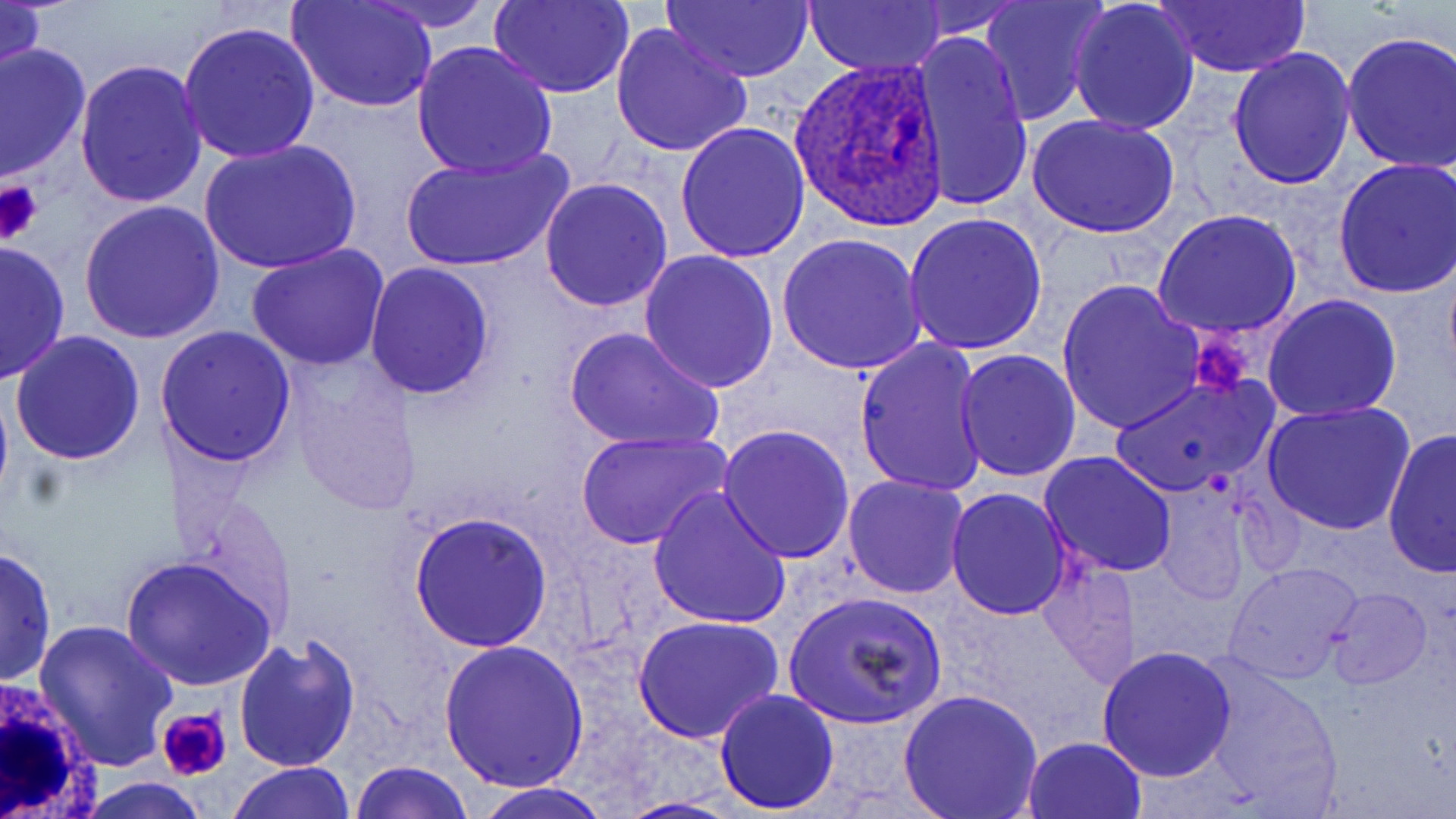

Approximate bounding boxes as (x1,y1)-(x2,y2) corner pairs in pixels. Platelet locations: (0,179)-(45,245), (1190,331)-(1255,399), (156,707)-(233,782). Plasmodium ovale-infected red blood cell locations: (790,57)-(950,229). White blood cell locations: (1,676)-(106,819). Uninfected red blood cell locations: (361,0)-(498,31), (490,0)-(633,99), (663,0)-(816,83), (805,0)-(946,77), (981,0)-(1106,124), (1068,0)-(1201,137), (1149,0)-(1312,76), (0,1)-(47,89), (289,1)-(439,113), (903,2)-(1029,39), (176,20)-(320,163), (610,24)-(752,158), (1341,30)-(1456,174), (911,31)-(1034,214), (412,40)-(557,179), (0,41)-(91,183), (1227,46)-(1356,190), (74,58)-(207,211), (1027,114)-(1179,241), (675,122)-(811,264), (198,138)-(362,274), (399,144)-(575,273), (1333,158)-(1456,301), (539,176)-(673,312), (77,199)-(226,344), (1152,208)-(1303,340), (902,214)-(1048,359), (777,235)-(926,376), (0,241)-(70,383), (248,243)-(387,371), (639,249)-(779,393), (365,262)-(496,400), (1056,278)-(1204,435), (1262,293)-(1403,423), (155,326)-(298,468), (563,327)-(724,455), (9,330)-(147,467), (855,339)-(988,496), (952,349)-(1082,483), (1113,375)-(1275,499), (1261,401)-(1415,538), (718,423)-(856,564), (1382,428)-(1456,578), (576,429)-(734,550), (1038,451)-(1178,577), (841,473)-(971,598), (1147,473)-(1264,599), (647,487)-(792,632), (945,487)-(1072,619), (407,510)-(553,653), (0,546)-(57,687), (1037,552)-(1140,687), (119,556)-(277,692), (1225,563)-(1363,684), (1327,585)-(1432,689), (783,589)-(949,732), (632,614)-(785,743), (33,619)-(177,769), (231,633)-(363,775), (438,638)-(591,792), (1096,644)-(1239,780), (1202,661)-(1343,814), (714,688)-(840,812), (897,688)-(1042,818), (1021,736)-(1148,819), (349,760)-(473,819), (227,761)-(356,818), (71,778)-(212,818), (469,782)-(617,819), (614,796)-(746,818). Slide-level diagnosis: Plasmodium ovale. 1000x magnification. Thin blood film. Optical microscopy. Image is 1456×819 pixels. May-Grünwald-Giemsa-stained preparation. One field of a larger specimen.